Classify this cell by malaria status.
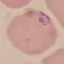

Parasitized.

Giemsa-stained preparation. Thin blood film. Acquired by smartphone through the microscope eyepiece. Automatically extracted cell patch, resized to 64 × 64 pixels.